Assess this cell for malaria.
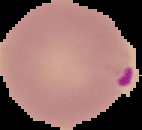
Parasitized.

Summary:
  - Image type: segmented cell region with the area outside set to black
  - Image size: 142×130 pixels
  - Preparation: thin blood film